Classify this cell by malaria status.
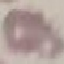
Uninfected.

Summary:
  - Image type: automatically extracted cell patch, resized to 64 × 64 pixels
  - Stain: Giemsa
  - Capture: smartphone through the microscope eyepiece
  - Preparation: thin smear